Report the malaria status of this cell.
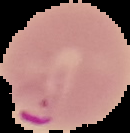

Parasitized.

Summary:
  - Image size: 130×133 pixels
  - Image type: segmented cell region on a black background
  - Preparation: thin blood smear